Name the blood parasite species.
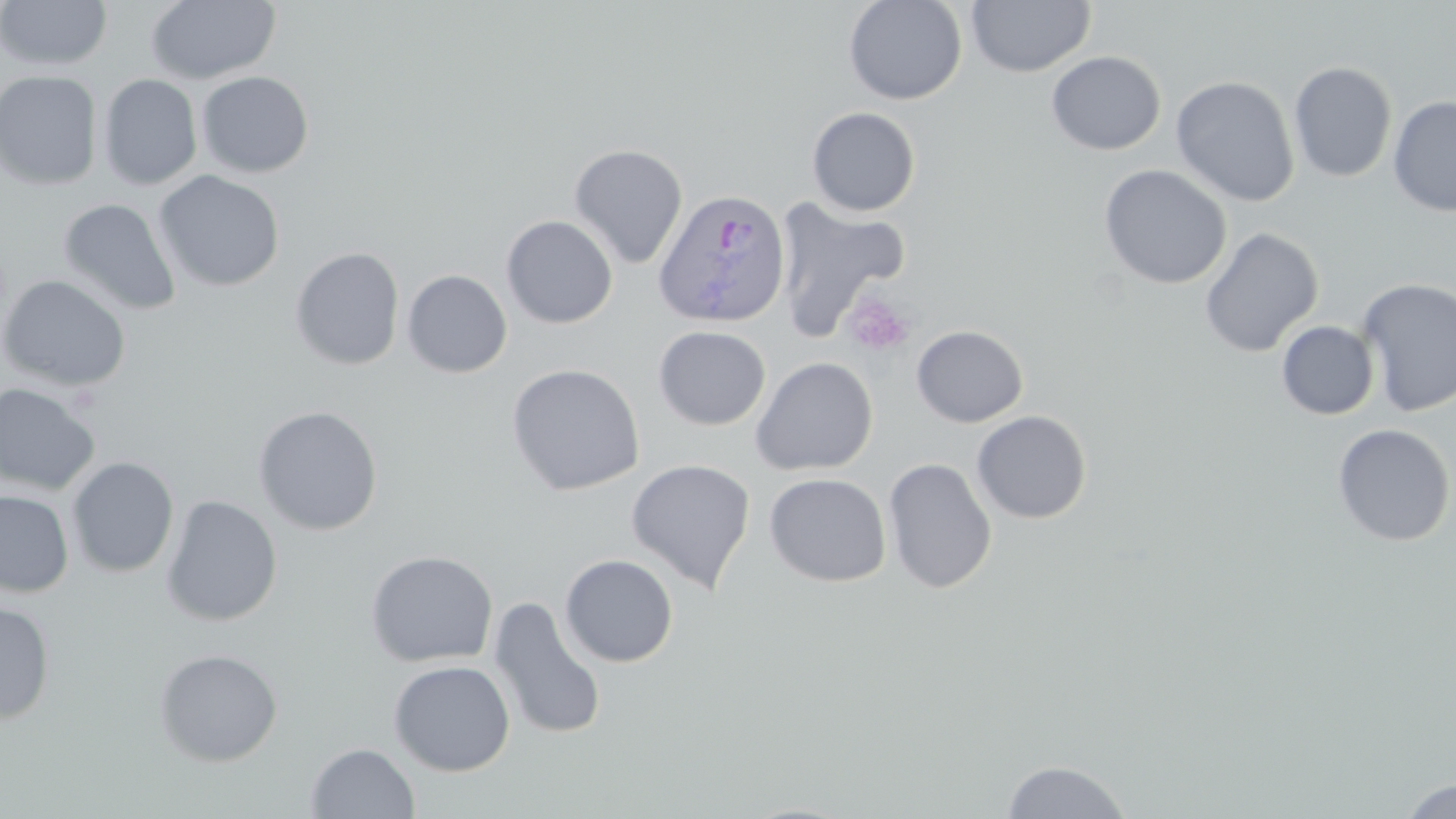
Plasmodium ovale.

Approximate bounding boxes as named x1/y1/x2/y2 corners in pixels. Plasmodium ovale-infected red blood cell locations: (x1=652, y1=187, x2=792, y2=329). Uninfected red blood cell locations: (x1=0, y1=0, x2=111, y2=71), (x1=146, y1=0, x2=282, y2=86), (x1=843, y1=0, x2=967, y2=105), (x1=966, y1=0, x2=1095, y2=78), (x1=1046, y1=50, x2=1166, y2=155), (x1=1288, y1=61, x2=1398, y2=183), (x1=0, y1=70, x2=103, y2=191), (x1=196, y1=71, x2=314, y2=178), (x1=98, y1=74, x2=202, y2=190), (x1=1171, y1=75, x2=1300, y2=207), (x1=1388, y1=96, x2=1456, y2=216), (x1=807, y1=107, x2=920, y2=216), (x1=569, y1=143, x2=689, y2=269), (x1=1098, y1=164, x2=1233, y2=290), (x1=153, y1=170, x2=285, y2=292), (x1=772, y1=197, x2=910, y2=341), (x1=58, y1=198, x2=181, y2=316), (x1=501, y1=215, x2=618, y2=329), (x1=1199, y1=227, x2=1324, y2=358), (x1=290, y1=246, x2=405, y2=370), (x1=402, y1=269, x2=513, y2=378), (x1=0, y1=274, x2=131, y2=393), (x1=1356, y1=277, x2=1456, y2=418), (x1=1276, y1=321, x2=1380, y2=420), (x1=653, y1=325, x2=772, y2=431), (x1=911, y1=325, x2=1029, y2=428), (x1=751, y1=356, x2=878, y2=477), (x1=506, y1=363, x2=646, y2=496), (x1=0, y1=382, x2=101, y2=496), (x1=252, y1=405, x2=384, y2=536), (x1=972, y1=410, x2=1092, y2=524), (x1=1332, y1=424, x2=1455, y2=547), (x1=66, y1=456, x2=180, y2=578), (x1=626, y1=458, x2=756, y2=594), (x1=883, y1=458, x2=998, y2=593), (x1=764, y1=472, x2=892, y2=587), (x1=0, y1=490, x2=74, y2=598), (x1=161, y1=495, x2=283, y2=627), (x1=365, y1=549, x2=499, y2=668), (x1=560, y1=554, x2=679, y2=667), (x1=488, y1=596, x2=608, y2=740), (x1=0, y1=601, x2=55, y2=724), (x1=153, y1=647, x2=283, y2=767), (x1=389, y1=660, x2=515, y2=776), (x1=306, y1=743, x2=420, y2=818), (x1=1001, y1=760, x2=1132, y2=818), (x1=1400, y1=778, x2=1456, y2=818). Platelet locations: (x1=843, y1=291, x2=916, y2=358). Single field of view. 1000x magnification. Image is 1456×819 pixels. Thin blood smear. May-Grünwald-Giemsa-stained preparation. Optical microscopy.